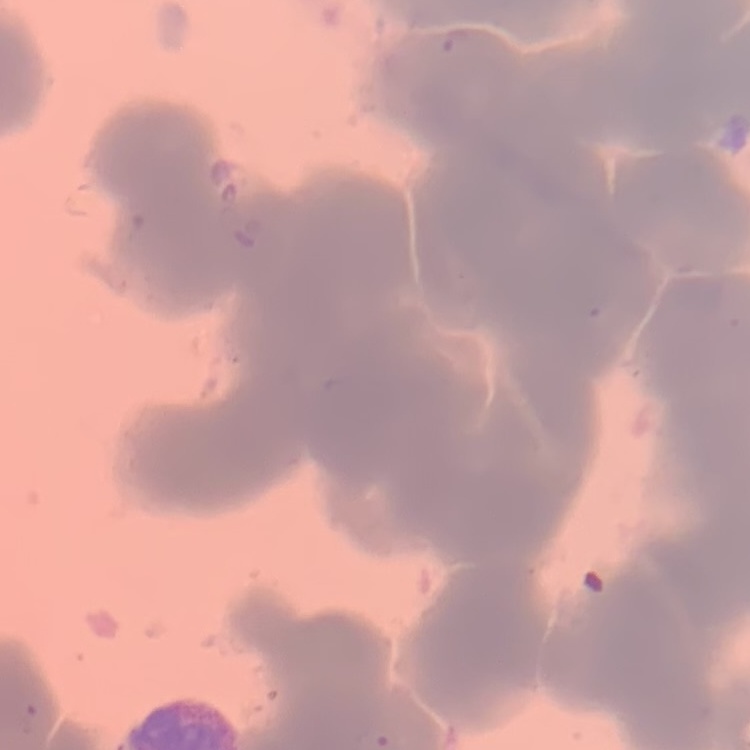 The erythrocytes show rouleaux formation. Thin blood film. Stained with either Field's or Giemsa. Square crop of a larger photomicrograph.